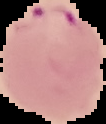

Summary:
  - Image size: 106×124 pixels
  - Preparation: thin blood smear
  - Result: malaria parasites identified
  - Image type: segmented cell region with the area outside set to black